State which cell type is depicted.
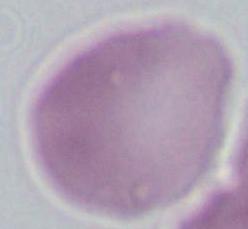
An erythrocyte.

{
  "magnification": "1000x",
  "modality": "micrograph"
}